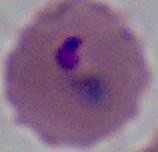

Summary:
  - Magnification: 400x or 1000x
  - Identification: Plasmodium
  - Modality: micrograph